Classify this cell by malaria status.
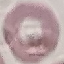
Uninfected.

Thin blood smear. Giemsa stain. Automatically extracted cell patch, resized to 64 × 64 pixels. Photographed with a smartphone camera at the microscope eyepiece.